Report the malaria status of this cell.
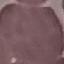

Uninfected.

Summary:
  - Stain: Giemsa
  - Capture: smartphone camera at the microscope eyepiece
  - Image type: cell patch, automatically extracted from a larger field of view and resized to 64 × 64 pixels
  - Preparation: thin blood film